Report the malaria status of this cell.
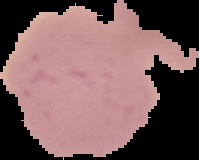
Uninfected.

image_size: 199×160 pixels
preparation: thin blood film
image_type: cell region segmented out of the field of view; surrounding area masked to black